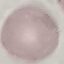

Summary:
  - Result: no malaria parasites seen
  - Preparation: thin blood smear
  - Image type: cell patch, automatically extracted from a larger field of view and resized to 64 × 64 pixels
  - Capture: smartphone camera at the microscope eyepiece
  - Stain: Giemsa